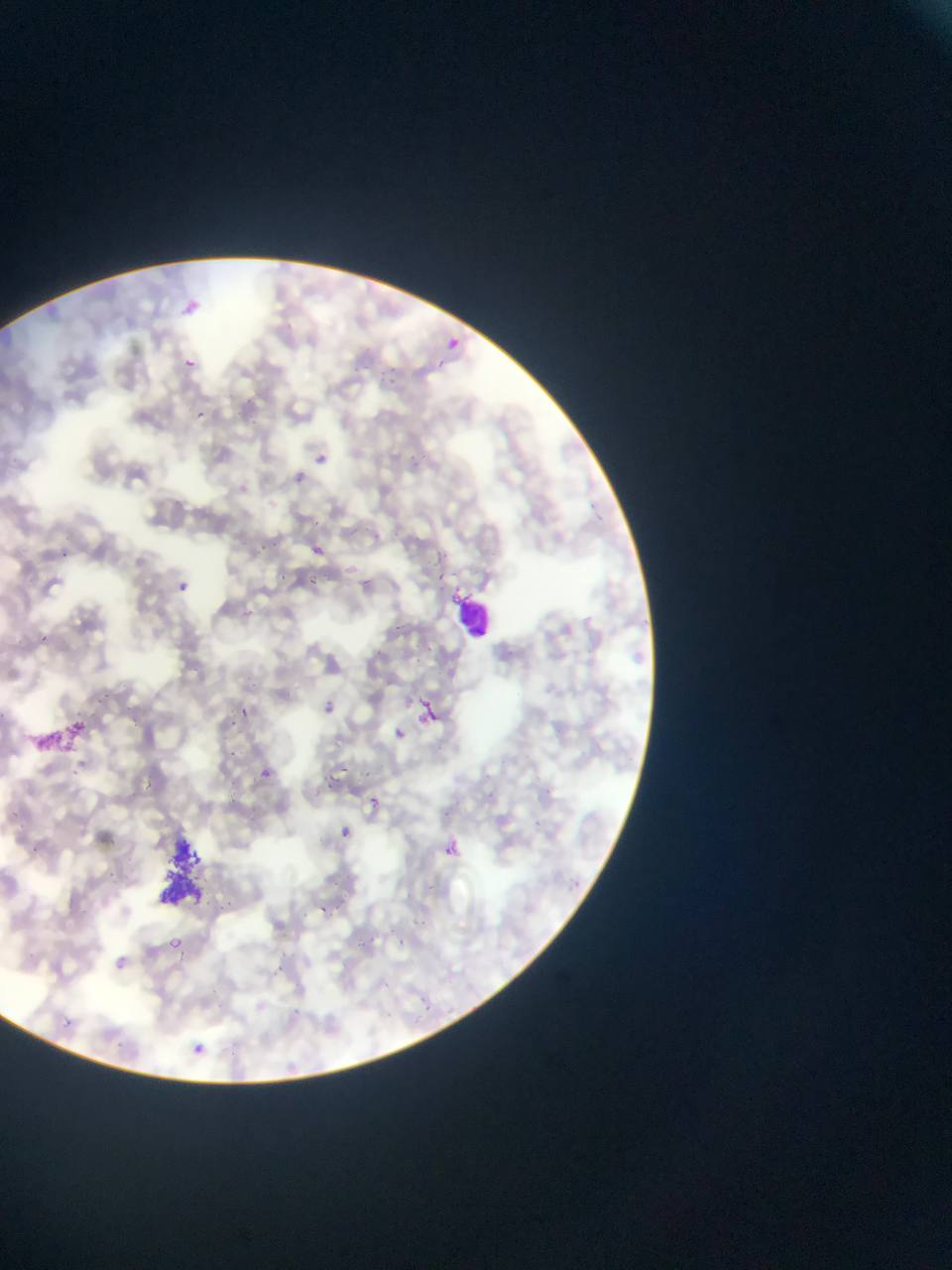

Approximate bounding boxes as [left, top, right, bottom] in pixels.
Summary:
  - Plasmodium parasite locations: [178, 298, 207, 315], [436, 332, 456, 350], [180, 350, 209, 372], [435, 357, 452, 370], [193, 408, 218, 424], [314, 447, 335, 471], [293, 466, 310, 492], [312, 545, 325, 556], [179, 577, 199, 605], [415, 691, 452, 737], [323, 694, 344, 716], [391, 722, 416, 752], [248, 760, 274, 780], [354, 778, 393, 809], [336, 822, 359, 846], [442, 838, 462, 858], [314, 898, 331, 914], [166, 933, 195, 954], [115, 952, 127, 970], [62, 1016, 75, 1027], [195, 1034, 223, 1058]
  - Leukocyte locations: [454, 590, 496, 635]
  - Field of view: single
  - Image size: 952×1270 pixels
  - Preparation: thin blood smear
  - Country: Ghana
  - Capture: mobile-phone photograph through a microscope